Comment on the morphology of the red blood cells.
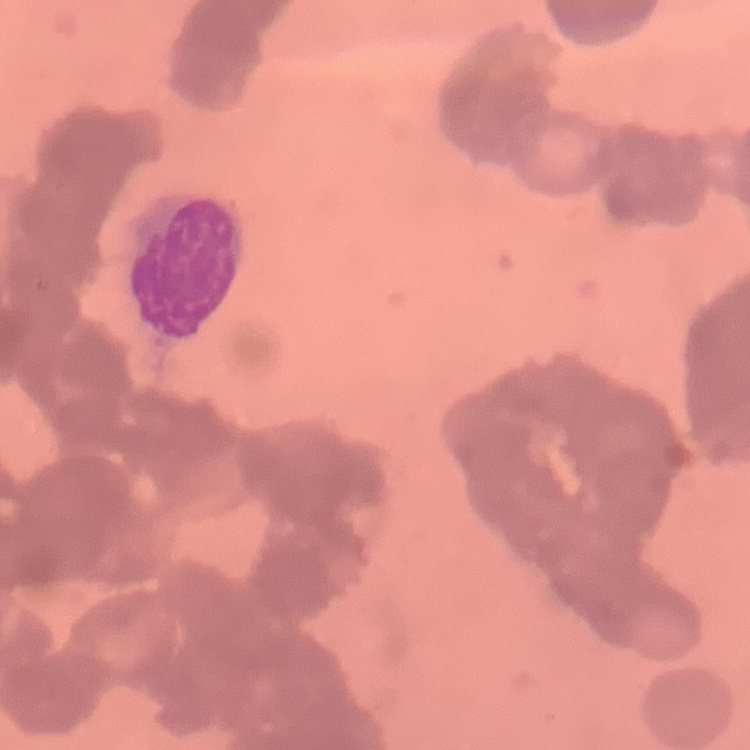

Rouleaux formation.

image type = square crop of a larger photomicrograph
preparation = thin blood film
stain = Field's or Giemsa